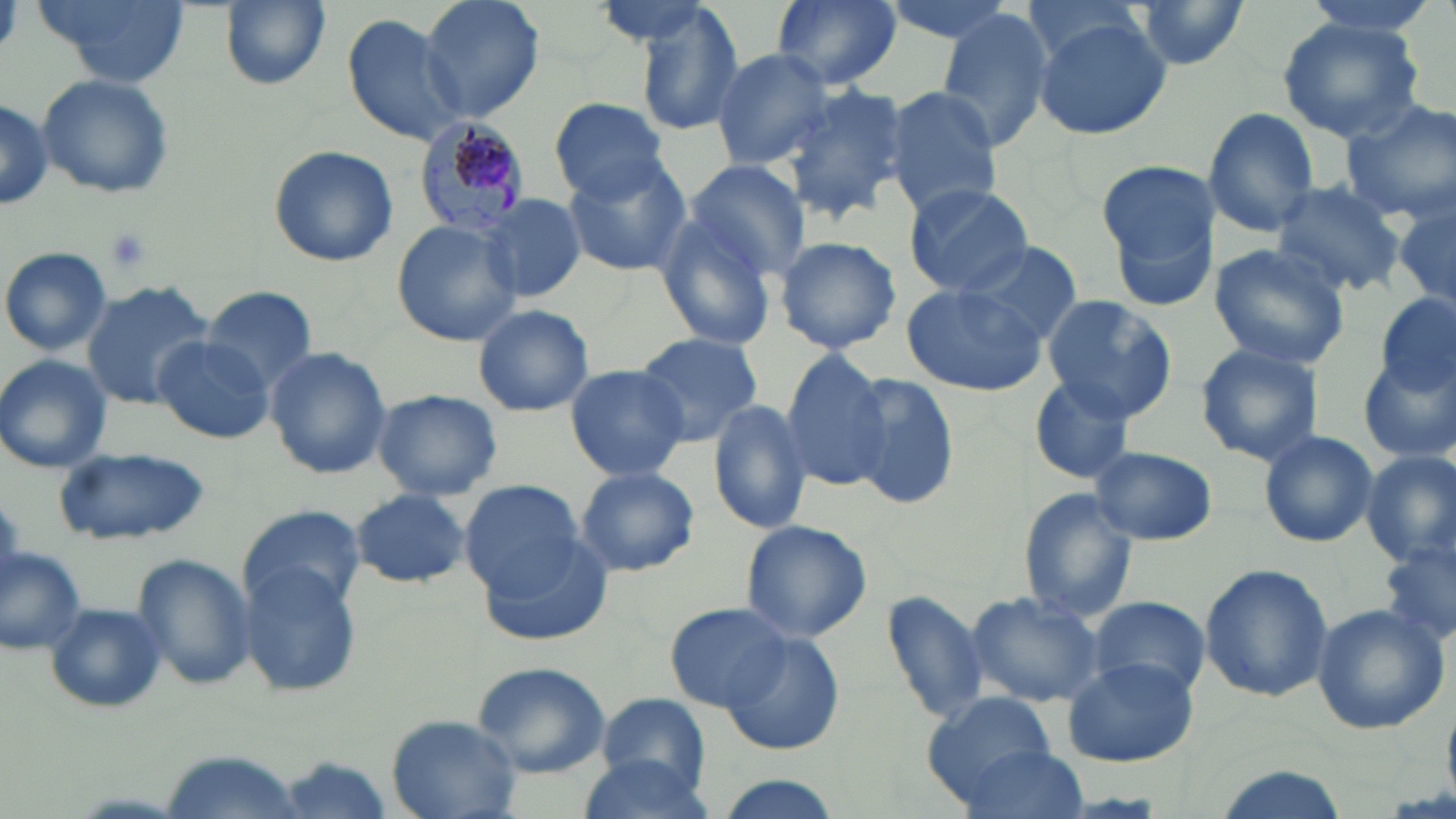

Summary:
  - Coordinate format: approximate bounding boxes as (x1,y1)-(x2,y2) corner pairs in pixels
  - Uninfected red blood cell locations: (41,0)-(190,89), (220,0)-(331,90), (419,0)-(546,122), (769,0)-(903,92), (875,0)-(1025,45), (1130,0)-(1250,69), (1296,0)-(1442,40), (1019,1)-(1150,66), (623,2)-(746,136), (934,8)-(1059,151), (341,13)-(470,147), (1031,16)-(1174,142), (1274,17)-(1428,144), (710,48)-(839,170), (37,73)-(174,199), (782,84)-(913,218), (882,86)-(1002,216), (0,95)-(52,209), (550,97)-(670,202), (1341,99)-(1456,223), (1203,107)-(1321,237), (267,144)-(399,268), (559,154)-(694,276), (684,159)-(810,281), (1098,160)-(1218,278), (1270,180)-(1406,299), (902,182)-(1034,296), (478,194)-(585,302), (1392,195)-(1455,315), (653,215)-(779,350), (392,221)-(523,346), (772,236)-(902,354), (957,240)-(1083,345), (1206,243)-(1351,371), (2,248)-(111,356), (80,280)-(215,408), (900,282)-(1045,396), (200,285)-(320,389), (1042,295)-(1177,421), (1376,295)-(1455,401), (473,304)-(594,416), (636,332)-(765,445), (153,335)-(273,443), (593,340)-(789,496), (1193,342)-(1325,466), (266,346)-(392,479), (777,353)-(892,490), (1359,354)-(1456,465), (0,355)-(113,473), (562,364)-(693,482), (842,371)-(961,510), (1027,372)-(1138,486), (369,390)-(506,501), (707,398)-(811,534), (1258,428)-(1379,548), (1091,445)-(1218,545), (55,447)-(211,544), (1360,450)-(1456,568), (576,466)-(699,577), (462,479)-(583,596), (349,488)-(471,588), (1018,490)-(1140,623), (237,506)-(364,616), (738,518)-(873,643), (475,533)-(616,649), (1380,540)-(1456,651), (0,545)-(89,656), (131,553)-(254,692), (238,559)-(361,696), (1199,562)-(1335,702), (882,588)-(990,722), (966,591)-(1104,709), (1090,595)-(1210,700), (43,601)-(166,713), (666,601)-(792,712), (1309,602)-(1448,736), (719,632)-(843,756), (1060,656)-(1199,768), (469,660)-(610,778), (922,692)-(1059,803), (589,693)-(717,796), (386,713)-(523,817), (959,744)-(1091,819), (163,751)-(304,817), (574,751)-(716,817), (274,755)-(395,819), (1212,766)-(1352,819), (711,775)-(843,819)
  - Platelet locations: (101,226)-(154,274)
  - Plasmodium malariae-infected red blood cell locations: (412,118)-(533,242)
  - Slide-level diagnosis: Plasmodium malariae
  - Image size: 1456×819 pixels
  - Magnification: 1000x
  - Field of view: one of a larger specimen
  - Modality: optical microscopy
  - Stain: May-Grünwald-Giemsa
  - Preparation: thin blood smear